Locate every cell, classifying each as a parasitized RBC, an uninfected RBC, or a WBC.
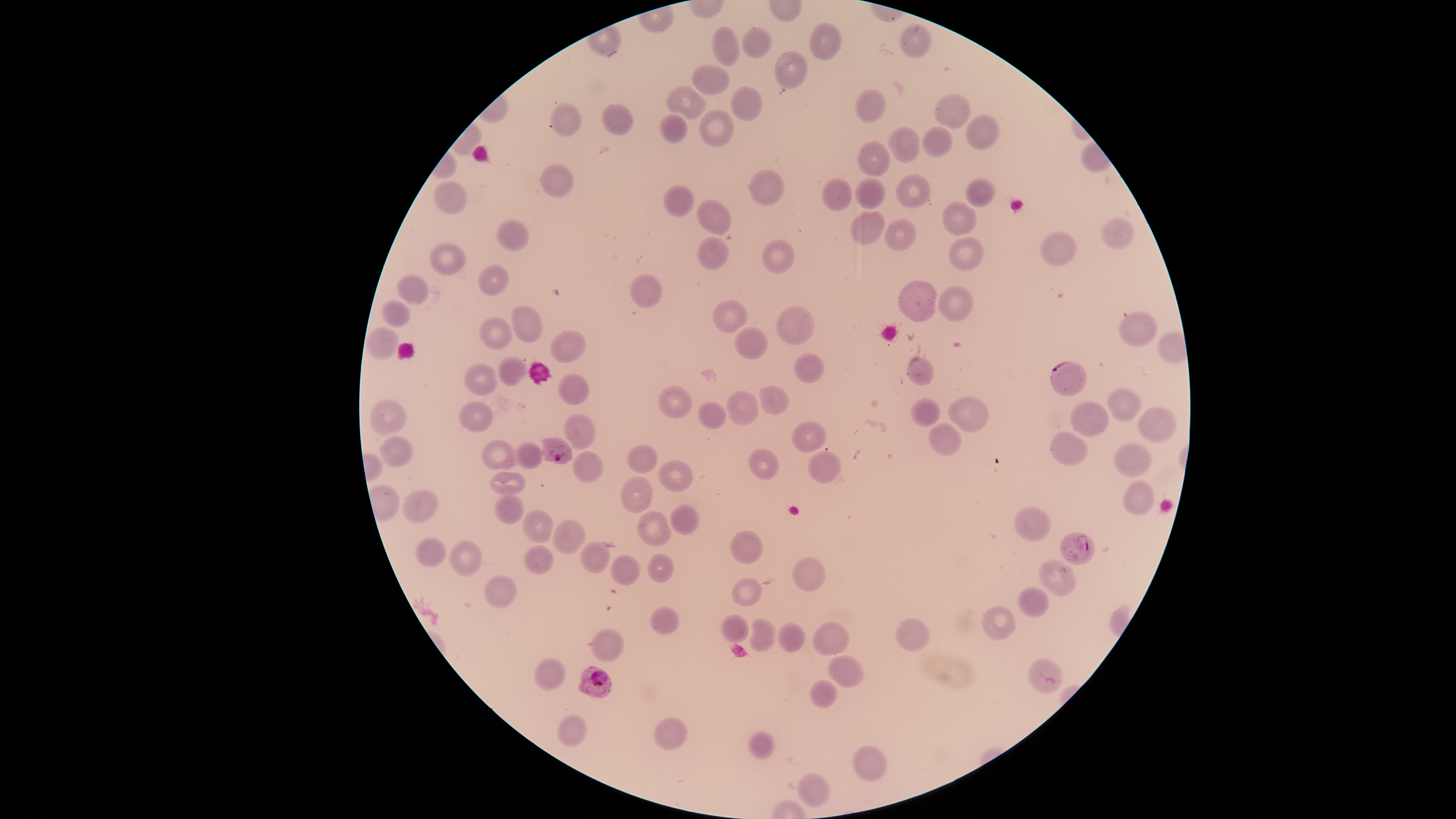
Approximate bounding boxes as {left, top, right, bottom} in pixels.
Parasitized RBCs: {1050, 361, 1086, 396}, {535, 438, 572, 463}, {1059, 533, 1094, 566}, {1028, 657, 1063, 695}, {578, 666, 612, 698}.
Uninfected RBCs: {809, 23, 842, 61}, {899, 24, 932, 57}, {712, 27, 741, 67}, {741, 28, 773, 59}, {775, 52, 808, 89}, {692, 65, 730, 95}, {667, 86, 705, 121}, {732, 87, 763, 121}, {856, 90, 887, 123}, {936, 94, 971, 129}, {550, 102, 583, 136}, {602, 103, 633, 136}, {701, 109, 734, 147}, {659, 114, 688, 144}, {967, 115, 1000, 151}, {922, 127, 954, 156}, {887, 128, 920, 163}, {857, 141, 892, 176}, {541, 164, 573, 197}, {749, 169, 784, 206}, {896, 174, 930, 208}, {855, 177, 885, 210}, {967, 178, 996, 207}, {433, 179, 467, 216}, {821, 180, 854, 210}, {664, 186, 695, 216}, {698, 199, 732, 234}, {942, 201, 977, 237}, {852, 212, 885, 245}, {1102, 218, 1135, 250}, {496, 219, 530, 251}, {883, 219, 917, 250}, {1039, 232, 1078, 267}, {697, 236, 729, 269}, {948, 237, 985, 271}, {762, 240, 795, 273}, {429, 242, 465, 276}, {477, 264, 509, 296}, {396, 275, 429, 304}, {631, 275, 662, 308}, {898, 281, 938, 323}, {938, 286, 974, 322}, {713, 299, 748, 333}, {381, 300, 411, 326}, {777, 305, 814, 346}, {511, 306, 543, 344}, {1119, 311, 1157, 346}, {481, 317, 513, 350}, {366, 327, 399, 360}, {734, 327, 768, 360}, {552, 329, 586, 363}, {794, 353, 824, 384}, {496, 356, 526, 386}, {907, 357, 935, 385}, {464, 364, 498, 395}, {559, 373, 588, 405}, {760, 385, 788, 415}, {659, 386, 692, 419}, {1108, 388, 1142, 421}, {727, 391, 759, 426}, {949, 396, 989, 432}, {911, 398, 942, 426}, {371, 399, 407, 436}, {700, 401, 727, 429}, {1069, 401, 1110, 437}, {458, 403, 493, 432}, {1139, 407, 1177, 442}, {563, 414, 596, 450}, {792, 421, 826, 452}, {928, 423, 961, 454}, {1050, 431, 1089, 465}, {380, 436, 413, 469}, {482, 440, 517, 469}, {1113, 442, 1152, 477}, {515, 443, 543, 470}, {628, 445, 658, 473}, {749, 449, 779, 482}, {809, 450, 842, 483}, {571, 452, 602, 484}, {658, 459, 694, 493}, {490, 472, 526, 495}, {622, 477, 652, 514}, {1124, 481, 1155, 515}, {402, 490, 439, 522}, {495, 494, 524, 525}, {670, 504, 699, 535}, {1014, 506, 1050, 542}, {523, 510, 553, 543}, {637, 511, 672, 547}, {552, 520, 585, 555}, {731, 531, 763, 565}, {415, 538, 447, 568}, {448, 540, 482, 577}, {579, 542, 611, 573}, {522, 546, 554, 574}, {648, 554, 674, 583}, {611, 555, 640, 586}, {792, 557, 827, 592}, {1038, 560, 1076, 597}, {484, 574, 517, 608}, {732, 578, 763, 606}, {1018, 586, 1049, 617}, {650, 607, 679, 635}, {981, 607, 1015, 640}, {720, 614, 749, 644}, {897, 618, 930, 652}, {748, 619, 776, 653}, {811, 621, 850, 655}, {777, 622, 806, 654}, {591, 629, 624, 662}, {830, 655, 865, 688}, {534, 658, 566, 690}, {810, 680, 838, 708}, {557, 714, 587, 746}, {654, 717, 688, 751}, {749, 731, 775, 759}, {854, 745, 887, 782}, {799, 772, 830, 807}.
No WBCs identified.

Thin smear of blood. Species: Plasmodium falciparum. The visible region is circular. Image is 1456×819 pixels. Giemsa stain. One field of view of the specimen. Photographed with a smartphone camera through the microscope eyepiece.